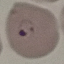
Summary:
  - Malaria status: parasitized
  - Stain: Giemsa
  - Image type: cell patch, automatically extracted from a larger field of view and resized to 64 × 64 pixels
  - Capture: smartphone through the microscope eyepiece
  - Preparation: thin blood smear